Name the parasite shown.
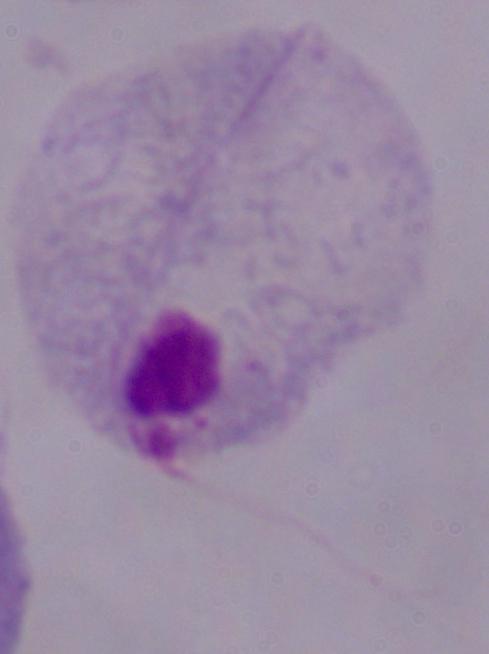

A trichomonad.

modality = photomicrograph
magnification = 1000x